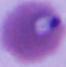

modality = photomicrograph
identification = Plasmodium
magnification = 400x or 1000x